Point out malaria parasites and leukocytes.
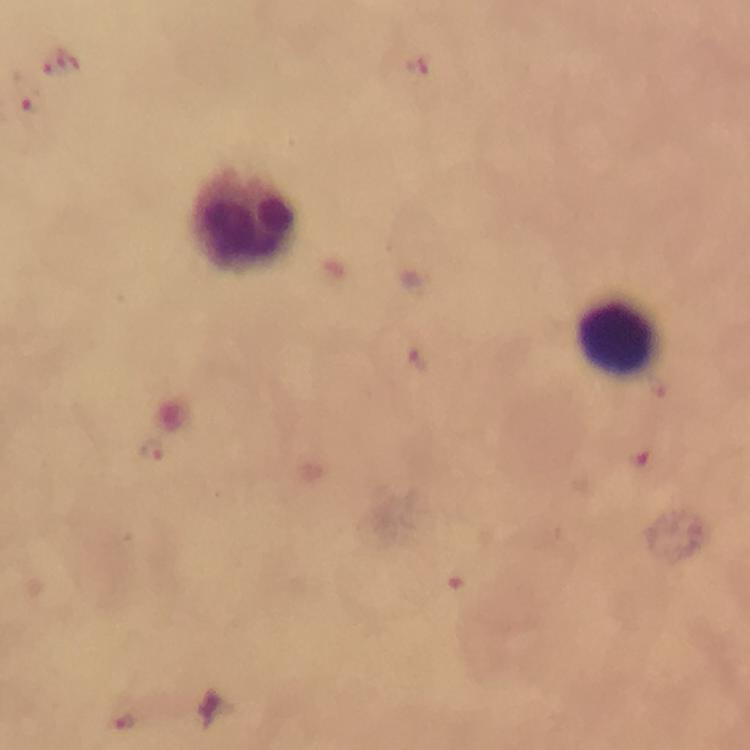
Approximate centers as {x, y} in pixels.
Malaria parasites: {60, 62}, {418, 68}, {26, 95}, {418, 362}, {155, 450}, {638, 457}, {449, 580}, {125, 717}.
Leukocytes: {243, 222}, {625, 336}.

Summary:
  - Preparation: thick blood smear
  - Context: from a malaria diagnostic workup
  - Immersion oil: applied
  - Magnification: 100x
  - Stain: Giemsa
  - Image size: 750×750 pixels
  - Cropped from: one field of view
  - Capture: smartphone photograph through a microscope